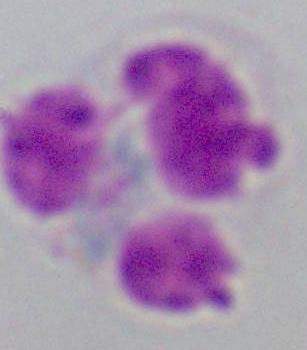

Summary:
  - Modality: photomicrograph
  - Magnification: 1000x
  - Identification: white blood cell